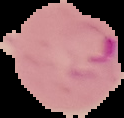
Summary:
  - Malaria status: parasitized
  - Image size: 124×118 pixels
  - Image type: cell region segmented out of the field of view; surrounding area masked to black
  - Preparation: thin blood smear